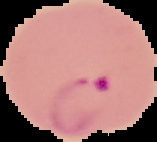
Summary:
  - Preparation: thin blood film
  - Image size: 157×142 pixels
  - Malaria status: parasitized
  - Image type: segmented cell region on a black background